Locate every Plasmodium falciparum-infected red blood cell.
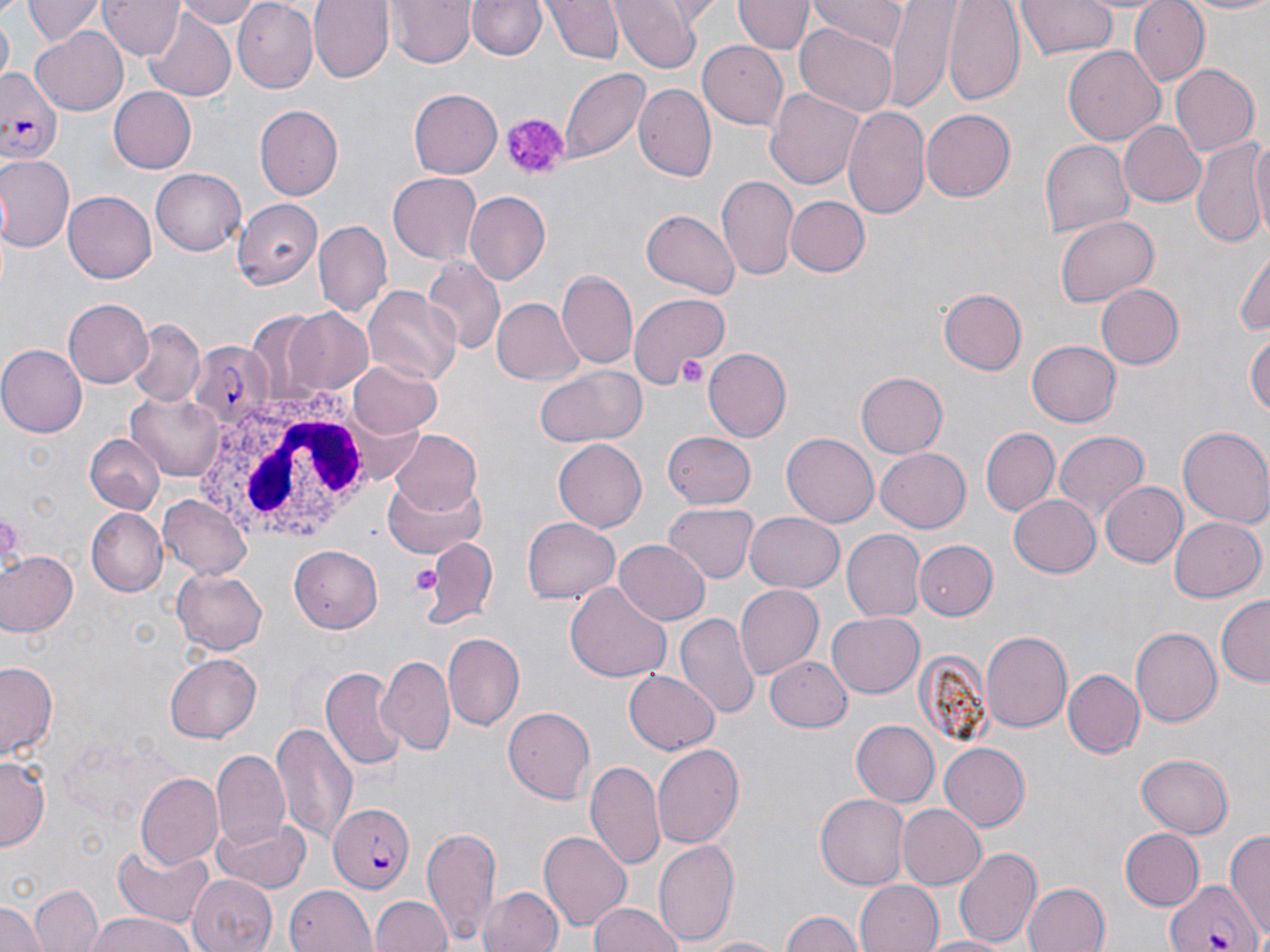

Approximate bounding boxes as (x1,y1)-(x2,y2) corner pairs in pixels.
Plasmodium falciparum-infected red blood cells: (0,67)-(64,159), (186,341)-(273,429), (329,801)-(415,893), (1164,878)-(1264,952).

Summary:
  - Uninfected red blood cell locations: (22,0)-(103,47), (100,0)-(182,59), (170,0)-(265,28), (309,0)-(394,83), (388,0)-(475,68), (468,0)-(543,61), (545,0)-(623,64), (736,0)-(811,55), (811,0)-(909,49), (944,0)-(1024,104), (1017,0)-(1118,60), (1129,0)-(1209,86), (1178,0)-(1270,16), (233,1)-(318,91), (612,1)-(703,72), (884,2)-(962,105), (143,8)-(239,100), (0,14)-(13,83), (795,24)-(899,117), (31,26)-(132,115), (700,41)-(790,131), (1064,44)-(1166,145), (1170,64)-(1259,156), (560,67)-(649,163), (633,84)-(717,183), (107,87)-(196,174), (766,87)-(866,191), (408,88)-(502,178), (842,103)-(931,220), (254,104)-(343,200), (921,108)-(1017,202), (1119,120)-(1208,208), (1248,131)-(1270,241), (1040,139)-(1133,236), (1191,140)-(1267,246), (0,155)-(74,250), (151,168)-(246,256), (389,172)-(483,265), (715,176)-(799,282), (63,192)-(156,283), (464,192)-(550,283), (228,195)-(325,291), (787,196)-(868,276), (641,207)-(738,296), (1056,215)-(1157,307), (314,219)-(391,318), (1233,248)-(1270,341), (424,260)-(505,357), (555,271)-(638,370), (1094,282)-(1185,370), (363,286)-(461,384), (939,288)-(1028,374), (628,294)-(729,394), (489,296)-(585,388), (61,299)-(151,388), (282,307)-(375,395), (130,320)-(204,406), (1247,329)-(1269,428), (1028,341)-(1121,426), (0,344)-(86,437), (702,345)-(795,441), (348,362)-(443,438), (534,364)-(647,447), (857,373)-(947,458), (128,391)-(228,481), (979,427)-(1060,516), (1054,427)-(1150,525), (1177,427)-(1270,528), (389,429)-(484,516), (663,429)-(757,508), (782,433)-(880,527), (84,435)-(163,513), (553,439)-(648,532), (875,448)-(972,532), (382,476)-(487,561), (1102,483)-(1185,567), (159,493)-(254,579), (1008,494)-(1101,578), (665,504)-(758,583), (86,508)-(168,595), (743,512)-(845,594), (1168,514)-(1265,602), (520,516)-(621,605), (842,528)-(925,620), (423,539)-(497,625), (614,539)-(709,624), (916,540)-(999,621), (289,546)-(384,633), (0,550)-(77,640), (172,569)-(268,654), (566,583)-(673,684), (735,584)-(824,679), (1218,597)-(1269,689), (827,612)-(926,698), (675,613)-(757,720), (1133,626)-(1225,727), (441,631)-(526,730), (979,631)-(1071,732), (165,653)-(262,742), (766,654)-(852,733), (380,656)-(454,754), (0,661)-(58,759), (322,667)-(408,771), (1062,668)-(1144,756), (625,671)-(720,754), (503,706)-(595,803), (850,720)-(939,807), (270,723)-(359,846), (938,741)-(1029,831), (650,745)-(746,848), (211,749)-(291,851), (1136,754)-(1233,838), (0,755)-(48,848), (586,761)-(667,873), (136,773)-(223,870), (815,791)-(910,886), (897,804)-(987,891), (213,817)-(308,893), (906,818)-(1019,918), (423,823)-(501,944), (1121,828)-(1205,910), (538,830)-(633,932), (1226,830)-(1270,941), (653,838)-(741,945), (111,843)-(214,928), (955,846)-(1041,949), (190,873)-(273,952), (853,880)-(943,952), (1022,881)-(1111,952), (30,884)-(102,952), (285,884)-(377,952), (479,886)-(564,952), (371,895)-(448,952), (0,899)-(46,952), (587,901)-(686,952), (781,910)-(862,952), (86,912)-(195,952), (694,934)-(787,952), (919,936)-(1012,952)
  - Platelet locations: (499,112)-(568,182), (676,354)-(707,391), (409,561)-(440,595)
  - White blood cell locations: (188,392)-(375,554)
  - Slide-level diagnosis: Plasmodium falciparum
  - Image size: 1270×952 pixels
  - Modality: optical microscopy
  - Stain: May-Grünwald-Giemsa
  - Field of view: one of a larger specimen
  - Magnification: 1000x
  - Preparation: thin blood smear